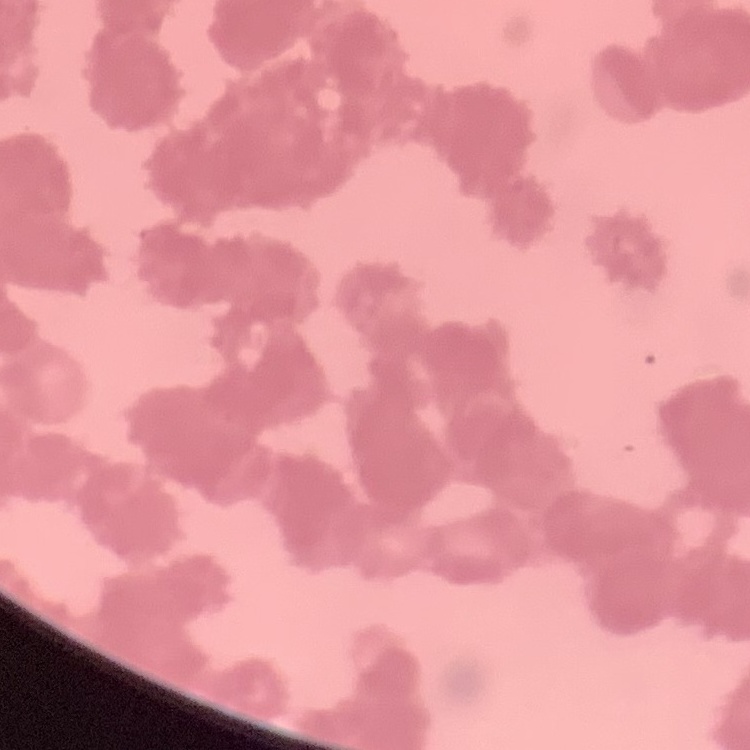

red blood cell morphology = rouleaux formation
preparation = thin blood film
stain = Field's or Giemsa
image type = one tile cut from a larger photomicrograph